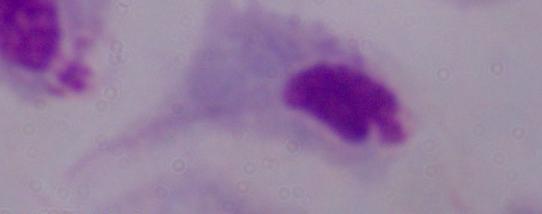 A trichomonad is shown. Photomicrograph. Captured at 1000x magnification.